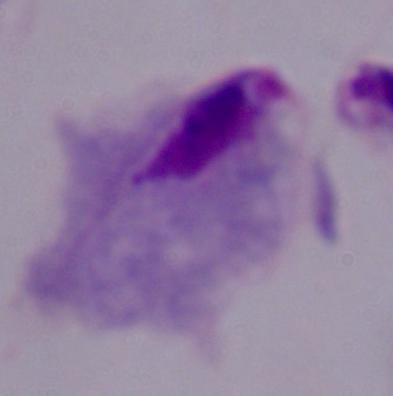

Summary:
  - Magnification: 1000x
  - Modality: photomicrograph
  - Identification: trichomonad